Assess the morphology of the erythrocytes.
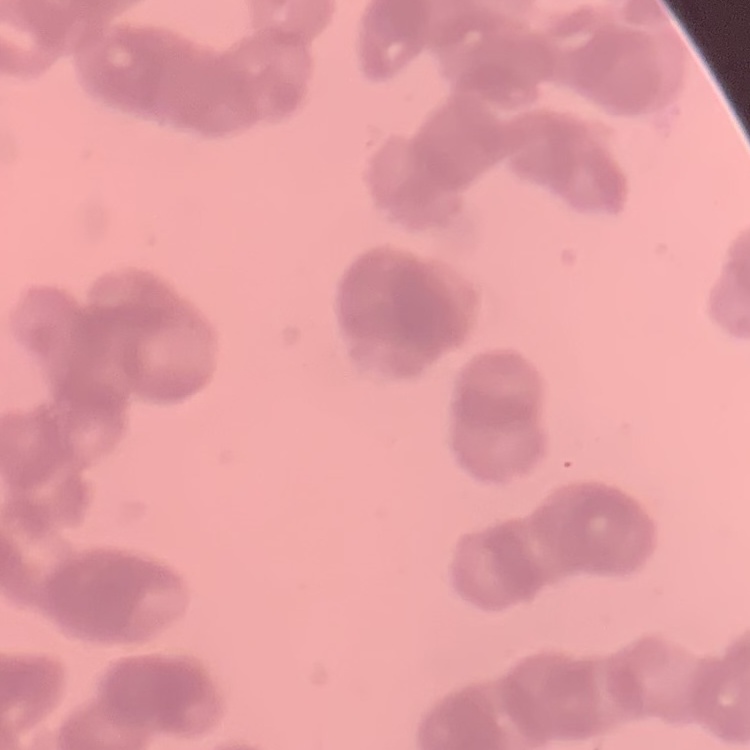
They show rouleaux formation.

Summary:
  - Preparation: thin blood film
  - Image type: one tile cut from a larger photomicrograph
  - Stain: Field's or Giemsa